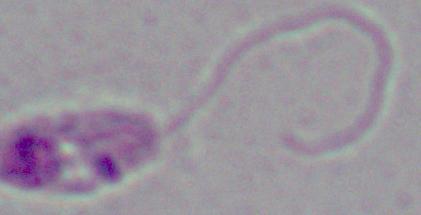
A Leishmania parasite is seen. Captured at 1000x magnification. Photomicrograph.